Locate and identify every blood parasite.
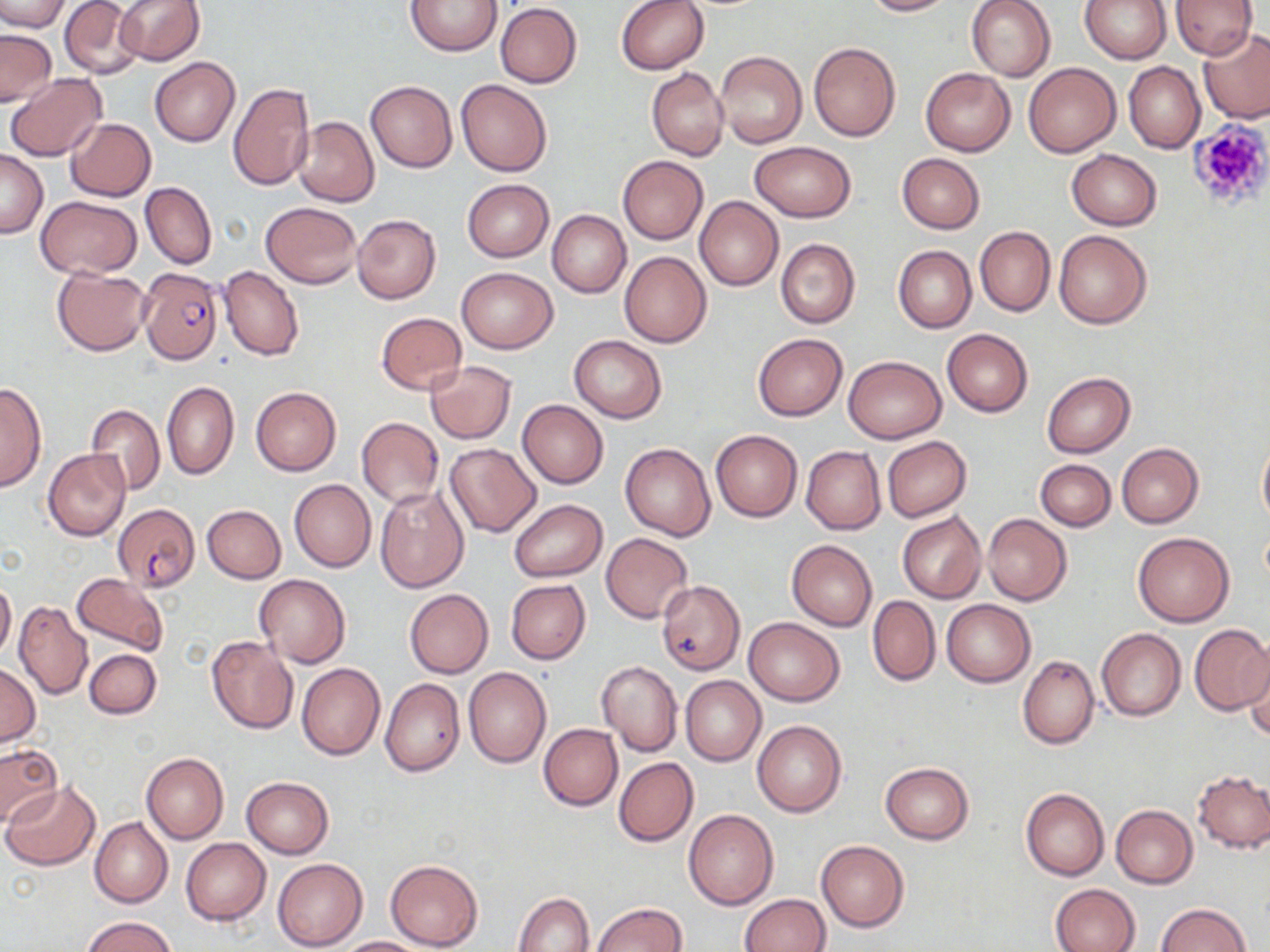
Approximate bounding boxes as (x1,y1)-(x2,y2) corner pairs in pixels.
Plasmodium falciparum-infected red blood cells: (139,267)-(222,363), (113,503)-(200,591).
No Plasmodium ovale, Plasmodium malariae, Plasmodium vivax, Babesia divergens, or Trypanosoma brucei observed.

Uninfected red blood cell locations: (0,0)-(69,33), (59,0)-(143,81), (113,0)-(205,66), (615,0)-(709,75), (861,0)-(957,16), (965,0)-(1056,81), (1082,0)-(1172,63), (1170,0)-(1257,59), (407,1)-(502,55), (495,3)-(582,87), (1198,27)-(1270,122), (0,30)-(57,105), (808,42)-(901,141), (714,50)-(807,149), (150,57)-(240,146), (1124,61)-(1205,153), (1022,62)-(1122,157), (921,67)-(1015,156), (647,68)-(728,161), (6,74)-(107,162), (456,80)-(552,177), (366,81)-(456,171), (228,82)-(315,191), (294,116)-(379,206), (66,118)-(156,200), (748,141)-(856,222), (1067,148)-(1162,229), (0,149)-(49,239), (897,153)-(985,232), (617,155)-(709,245), (462,179)-(554,262), (140,182)-(217,269), (36,196)-(142,277), (694,196)-(784,290), (261,202)-(361,288), (547,210)-(631,296), (352,214)-(441,303), (975,226)-(1054,316), (1053,230)-(1152,329), (775,238)-(861,328), (893,245)-(976,332), (620,251)-(712,347), (219,266)-(304,361), (52,267)-(151,354), (456,267)-(558,353), (375,312)-(467,394), (942,329)-(1033,417), (753,333)-(848,420), (568,336)-(667,422), (842,356)-(947,444), (425,360)-(517,443), (1042,372)-(1135,457), (162,382)-(239,480), (0,383)-(46,494), (250,387)-(341,476), (516,400)-(607,489), (86,402)-(164,496), (356,417)-(443,507), (711,430)-(803,522), (1257,435)-(1270,529), (881,436)-(972,523), (445,443)-(541,537), (621,443)-(715,541), (1116,443)-(1204,528), (801,446)-(885,534), (43,449)-(131,541), (1035,460)-(1115,531), (290,479)-(376,572), (374,484)-(471,593), (508,499)-(608,581), (202,504)-(286,582), (897,511)-(986,604), (984,514)-(1072,605), (1132,530)-(1235,627), (600,532)-(693,623), (786,539)-(876,631), (71,573)-(170,656), (255,573)-(350,668), (0,577)-(16,661), (505,580)-(591,664), (657,581)-(745,675), (405,590)-(493,678), (868,595)-(939,686), (942,599)-(1034,687), (14,600)-(92,701), (744,618)-(844,706), (1188,624)-(1270,715), (1096,628)-(1186,721), (207,635)-(298,734), (83,648)-(161,719), (1244,651)-(1270,743), (1018,655)-(1099,749), (596,660)-(682,756), (296,662)-(385,761), (0,663)-(39,745), (464,667)-(551,768), (680,675)-(766,766), (380,678)-(465,776), (751,718)-(847,817), (538,723)-(623,810), (0,744)-(61,825), (141,753)-(229,844), (613,756)-(698,847), (880,761)-(974,844), (1193,771)-(1270,853), (241,777)-(334,858), (3,781)-(100,870), (1020,788)-(1110,881), (1110,805)-(1197,888), (684,809)-(778,910), (90,816)-(171,908), (181,838)-(270,926), (816,840)-(909,931), (272,858)-(367,950), (384,859)-(483,951), (1051,883)-(1141,952), (514,891)-(595,952), (740,894)-(831,952), (592,903)-(688,951), (1155,904)-(1251,952), (83,916)-(175,952), (336,935)-(431,951). Platelet locations: (1185,120)-(1270,209). Slide-level diagnosis: Plasmodium falciparum. Thin blood film. Optical microscopy. Image is 1270×952 pixels. May-Grünwald-Giemsa-stained preparation. One field of a larger specimen. Captured at 1000x magnification.